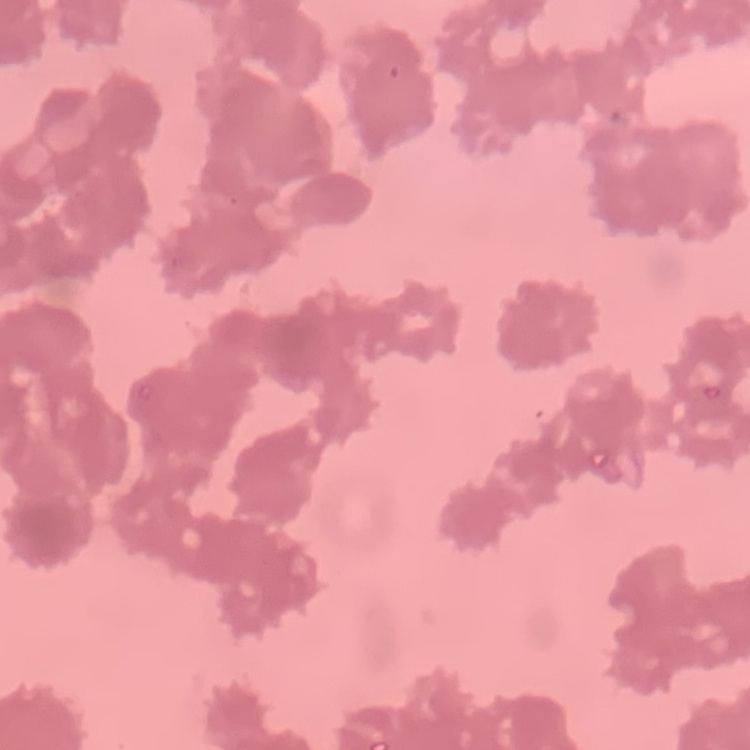

Summary:
  - Red blood cell morphology: rouleaux formation
  - Stain: Field's or Giemsa
  - Preparation: thin blood smear
  - Image type: square crop of a larger photomicrograph